Outline each blood parasite and name the species.
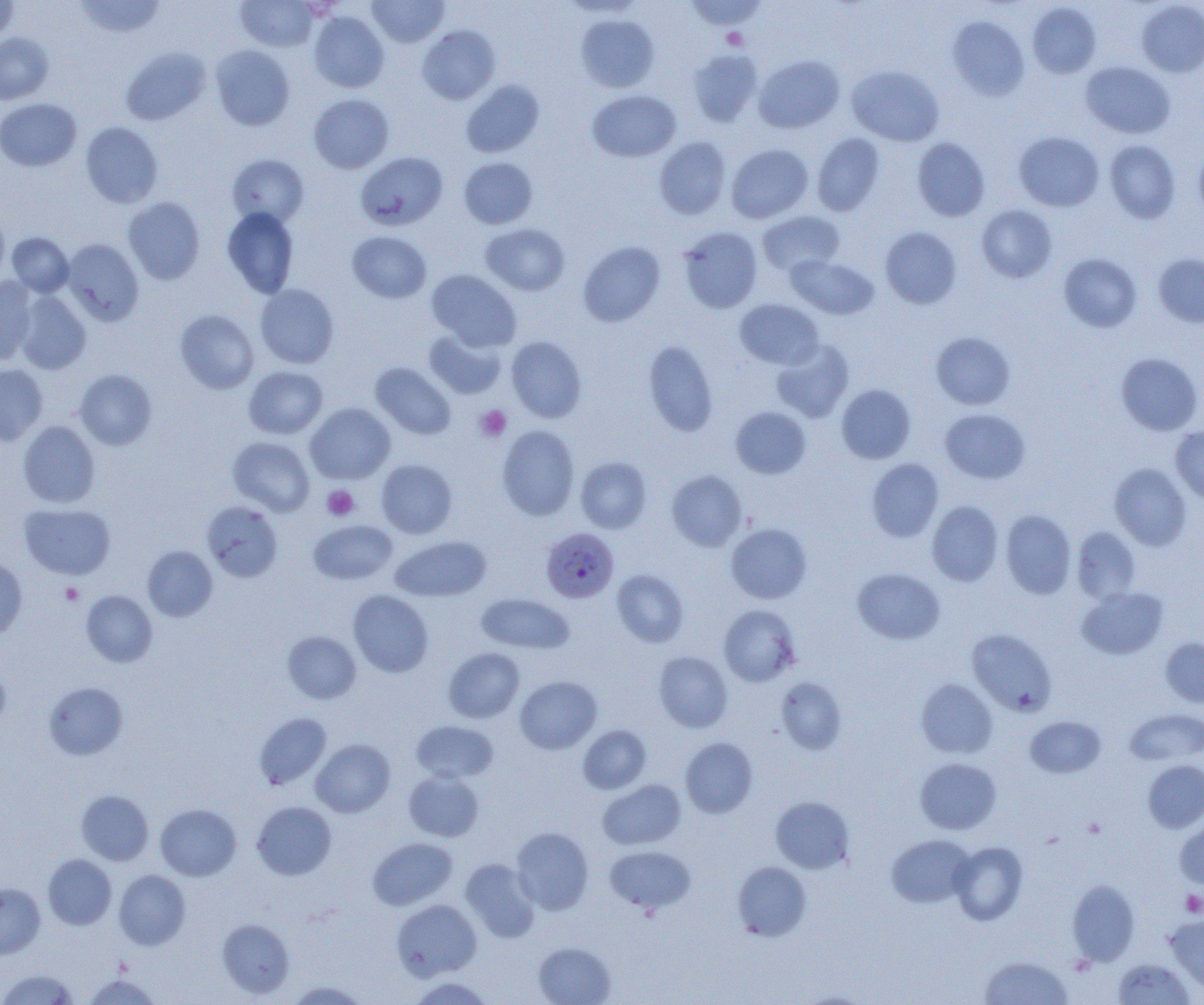

Approximate bounding boxes as [x1, y1, x2, y2] in pixels.
Plasmodium falciparum-infected red blood cells: [541, 527, 619, 603].
No Plasmodium ovale, Plasmodium malariae, Plasmodium vivax, Babesia divergens, or Trypanosoma brucei observed.

Platelet locations: [721, 28, 749, 50], [475, 405, 511, 442], [322, 485, 359, 521], [60, 582, 84, 605], [1181, 890, 1204, 917]. Uninfected red blood cell locations: [0, 0, 19, 44], [74, 0, 167, 38], [236, 0, 318, 51], [367, 0, 449, 47], [682, 0, 768, 31], [1136, 1, 1204, 78], [1027, 3, 1102, 78], [309, 11, 389, 92], [575, 14, 660, 92], [948, 15, 1029, 101], [417, 25, 500, 104], [0, 32, 54, 104], [210, 44, 295, 130], [121, 47, 210, 125], [687, 49, 763, 127], [754, 54, 845, 133], [1080, 61, 1175, 139], [846, 64, 945, 146], [460, 80, 545, 158], [587, 89, 681, 162], [308, 93, 394, 173], [0, 98, 82, 171], [80, 122, 163, 208], [1014, 131, 1104, 212], [812, 133, 885, 217], [654, 137, 731, 219], [912, 137, 991, 221], [1105, 140, 1181, 224], [1193, 142, 1204, 222], [726, 143, 814, 223], [355, 151, 448, 231], [227, 153, 309, 227], [459, 157, 538, 229], [123, 197, 205, 284], [976, 204, 1057, 283], [222, 207, 300, 298], [757, 210, 845, 277], [0, 212, 9, 287], [480, 223, 571, 296], [677, 226, 763, 313], [879, 226, 962, 309], [347, 231, 432, 303], [7, 232, 74, 297], [62, 238, 144, 326], [578, 241, 666, 327], [1058, 253, 1142, 332], [1153, 253, 1204, 327], [785, 254, 879, 319], [426, 269, 521, 351], [0, 276, 38, 363], [254, 283, 340, 369], [15, 291, 92, 374], [734, 298, 824, 370], [174, 309, 259, 394], [424, 328, 508, 399], [930, 331, 1016, 410], [424, 335, 586, 409], [505, 336, 587, 423], [771, 339, 855, 422], [643, 340, 719, 437], [1116, 352, 1203, 436], [370, 362, 456, 440], [0, 363, 48, 446], [243, 366, 328, 439], [75, 369, 157, 450], [836, 384, 916, 464], [305, 402, 395, 484], [730, 406, 811, 479], [940, 408, 1030, 483], [18, 421, 101, 508], [497, 425, 580, 520], [1170, 426, 1204, 505], [228, 436, 315, 517], [575, 456, 652, 534], [866, 458, 944, 542], [376, 459, 457, 538], [1109, 463, 1192, 550], [665, 470, 748, 551], [927, 500, 1003, 586], [202, 501, 283, 582], [20, 503, 116, 580], [1000, 510, 1076, 598], [308, 519, 398, 585], [725, 523, 812, 604], [1072, 526, 1141, 604], [390, 535, 491, 602], [142, 545, 217, 622], [0, 556, 28, 639], [852, 568, 945, 644], [612, 569, 689, 647], [1076, 586, 1168, 660], [81, 590, 157, 667], [348, 590, 433, 677], [477, 593, 574, 655], [718, 604, 801, 686], [966, 628, 1058, 716], [282, 631, 361, 704], [1160, 637, 1204, 708], [444, 648, 524, 723], [653, 651, 733, 732], [0, 663, 11, 730], [515, 676, 602, 754], [776, 677, 848, 754], [915, 678, 998, 759], [44, 682, 127, 759], [1125, 708, 1204, 766], [254, 712, 332, 789], [1026, 715, 1106, 778], [411, 720, 499, 783], [578, 725, 651, 794], [680, 737, 757, 818], [311, 739, 395, 817], [915, 757, 1002, 835], [1143, 760, 1204, 833], [403, 770, 484, 842], [597, 779, 686, 850], [76, 790, 153, 865], [770, 796, 855, 874], [251, 801, 337, 880], [155, 804, 241, 881], [1175, 814, 1204, 889], [511, 827, 594, 914], [886, 834, 975, 908], [367, 837, 457, 910], [949, 841, 1028, 925], [605, 845, 696, 914], [43, 854, 116, 929], [460, 858, 540, 943], [732, 860, 811, 941], [114, 870, 190, 949], [1067, 879, 1140, 965], [0, 883, 45, 958], [392, 899, 482, 980], [1165, 914, 1204, 993], [217, 919, 295, 998], [533, 941, 616, 1005], [979, 954, 1072, 1004], [1112, 958, 1195, 1004], [1, 969, 78, 1004], [83, 974, 161, 1004], [408, 976, 494, 1005], [286, 980, 370, 1004]. Slide-level diagnosis: Plasmodium falciparum. Single field of view. Light microscopy. Image is 1204×1005 pixels. 1000x magnification. Thin blood smear.